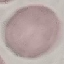
malaria status = uninfected
capture = smartphone through the microscope eyepiece
preparation = thin blood smear
stain = Giemsa
image type = cell patch, automatically extracted from a larger field of view and resized to 64 × 64 pixels